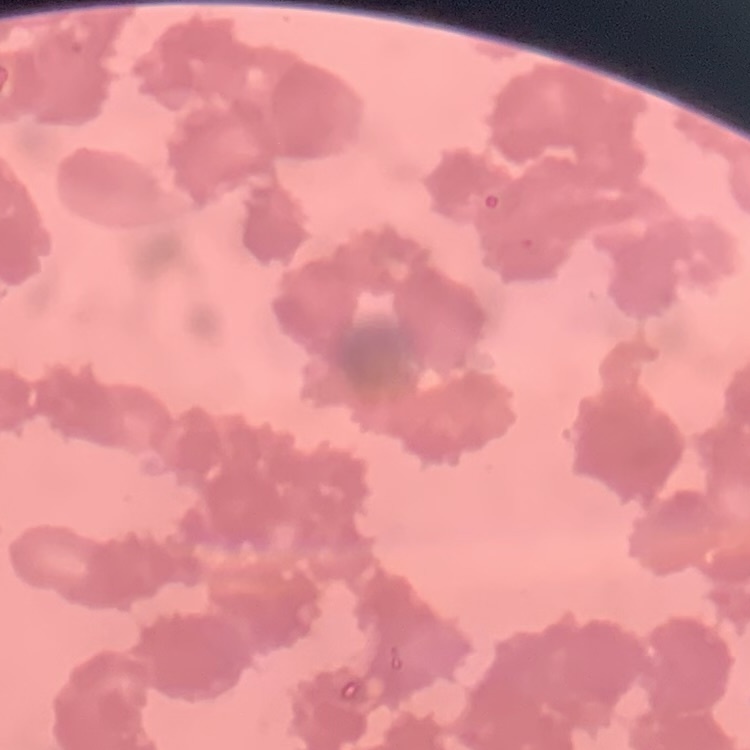 The red blood cells show rouleaux formation. Thin blood film. Field's or Giemsa stain. One tile cut from a larger photomicrograph.